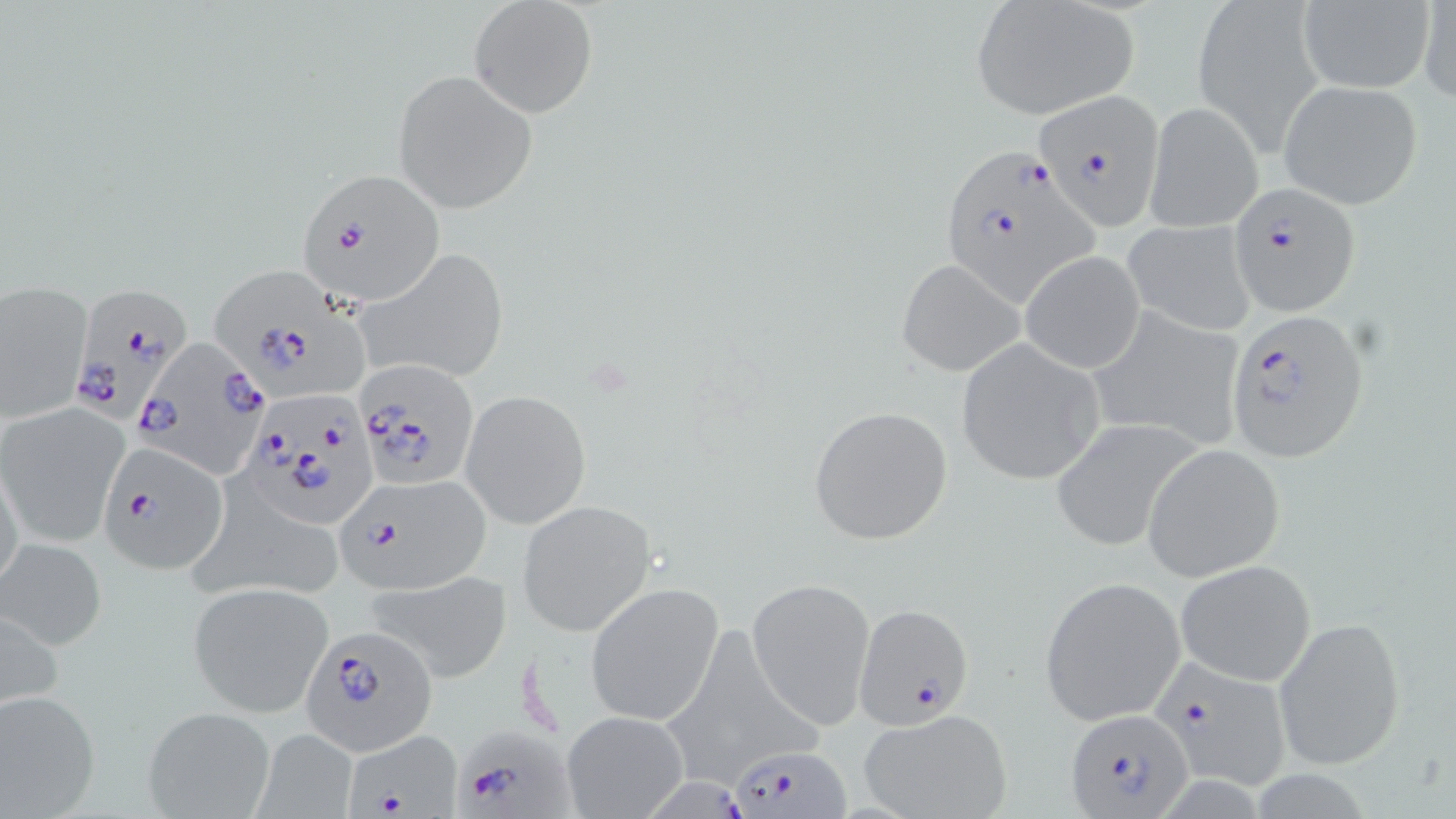
slide-level diagnosis = Plasmodium falciparum
preparation = thin blood smear
field of view = single
Plasmodium falciparum-infected red blood cell locations = approximate bounding boxes as (x1, y1, x2, y2) in pixels: (1034, 92, 1167, 229), (934, 146, 1099, 308), (296, 168, 446, 309), (1232, 183, 1360, 317), (214, 265, 374, 397), (64, 281, 194, 428), (1226, 309, 1369, 458), (136, 339, 273, 502), (355, 359, 480, 492), (240, 390, 377, 528), (98, 442, 228, 577), (334, 472, 492, 593), (853, 602, 974, 727), (303, 625, 438, 755), (1152, 655, 1297, 791), (1064, 709, 1194, 817), (448, 721, 575, 819), (346, 732, 463, 819), (731, 742, 848, 816), (650, 770, 753, 819)
modality = light microscopy
magnification = 1000x
uninfected red blood cell locations = approximate bounding boxes as (x1, y1, x2, y2) in pixels: (1195, 0, 1323, 146), (1416, 0, 1456, 106), (1295, 1, 1437, 93), (468, 2, 597, 119), (970, 2, 1140, 119), (391, 71, 536, 212), (1278, 80, 1424, 209), (1143, 100, 1262, 232), (1122, 220, 1256, 336), (358, 249, 509, 384), (1019, 251, 1146, 374), (896, 258, 1025, 378), (0, 283, 90, 422), (1084, 306, 1247, 454), (956, 339, 1107, 486), (461, 390, 591, 529), (1, 403, 128, 548), (807, 404, 955, 546), (1049, 419, 1203, 553), (1142, 444, 1286, 582), (0, 466, 26, 598), (186, 486, 351, 606), (517, 499, 657, 636), (1, 538, 108, 652), (1175, 559, 1317, 686), (371, 571, 512, 678), (746, 577, 875, 729), (1039, 577, 1186, 724), (585, 582, 726, 727), (188, 583, 332, 716), (1274, 613, 1405, 772), (660, 625, 819, 788), (0, 689, 101, 817), (142, 705, 276, 819), (859, 708, 1014, 819), (561, 709, 689, 818), (253, 730, 359, 818)
stain = May-Grünwald-Giemsa
image size = 1456×819 pixels